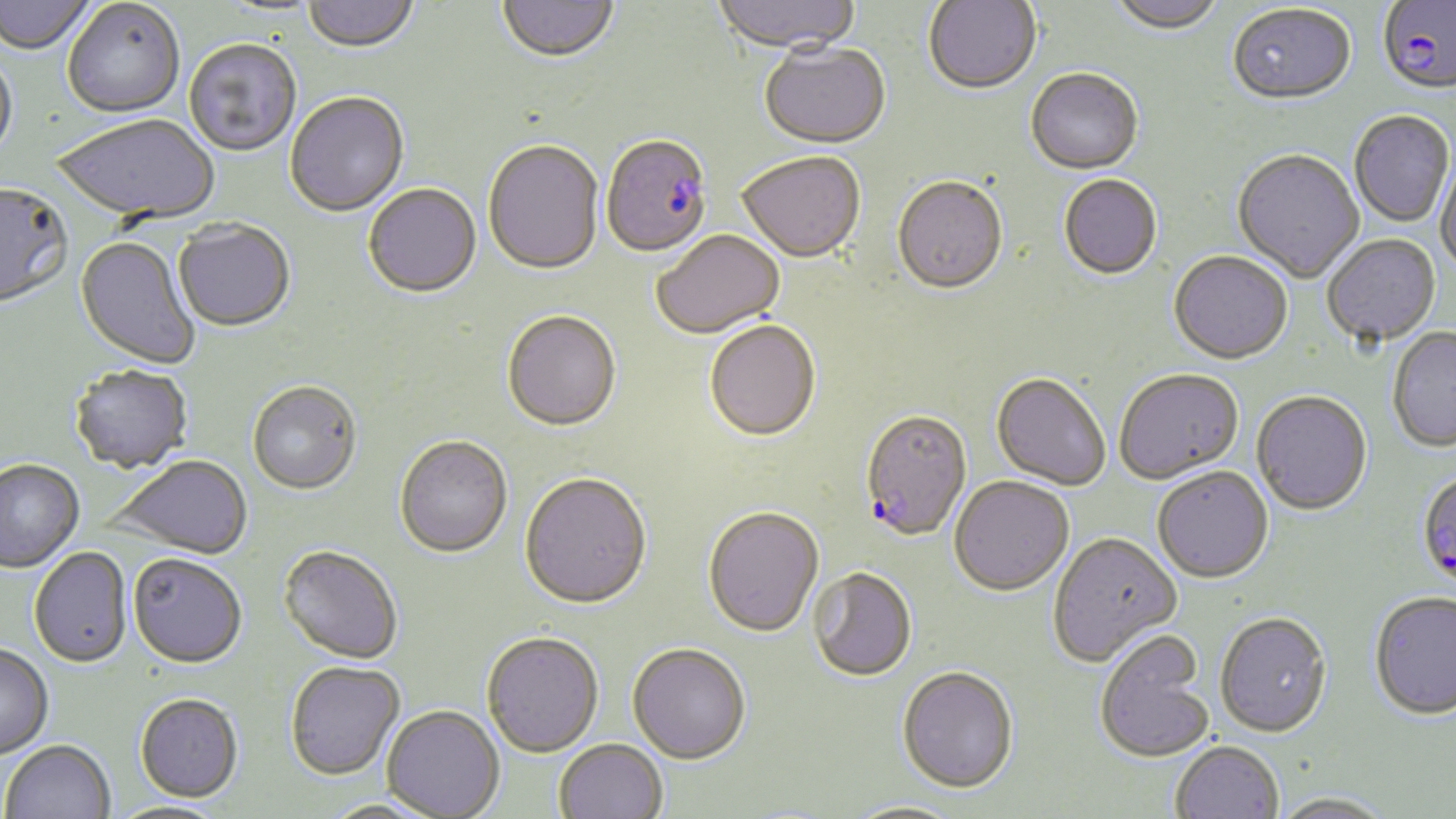

Approximate bounding boxes as named x1/y1/x2/y2 corners in pixels. Uninfected red blood cell locations: (x1=0, y1=0, x2=98, y2=57), (x1=304, y1=0, x2=418, y2=55), (x1=498, y1=0, x2=619, y2=66), (x1=711, y1=0, x2=863, y2=57), (x1=923, y1=0, x2=1042, y2=97), (x1=1108, y1=0, x2=1226, y2=37), (x1=62, y1=1, x2=185, y2=120), (x1=214, y1=1, x2=328, y2=20), (x1=1227, y1=6, x2=1356, y2=108), (x1=183, y1=41, x2=301, y2=158), (x1=759, y1=45, x2=891, y2=151), (x1=0, y1=55, x2=18, y2=170), (x1=1026, y1=71, x2=1144, y2=177), (x1=285, y1=94, x2=409, y2=219), (x1=1349, y1=113, x2=1454, y2=229), (x1=54, y1=117, x2=219, y2=225), (x1=483, y1=142, x2=604, y2=278), (x1=1232, y1=151, x2=1365, y2=284), (x1=1435, y1=152, x2=1456, y2=276), (x1=737, y1=154, x2=865, y2=265), (x1=1059, y1=176, x2=1162, y2=282), (x1=892, y1=179, x2=1008, y2=298), (x1=363, y1=185, x2=482, y2=301), (x1=0, y1=186, x2=73, y2=311), (x1=173, y1=221, x2=296, y2=334), (x1=652, y1=232, x2=786, y2=341), (x1=1322, y1=236, x2=1441, y2=348), (x1=74, y1=237, x2=200, y2=371), (x1=1168, y1=253, x2=1293, y2=367), (x1=502, y1=313, x2=621, y2=434), (x1=704, y1=322, x2=821, y2=444), (x1=1387, y1=328, x2=1456, y2=455), (x1=69, y1=366, x2=193, y2=475), (x1=1115, y1=371, x2=1243, y2=486), (x1=990, y1=374, x2=1110, y2=492), (x1=247, y1=383, x2=362, y2=496), (x1=1251, y1=393, x2=1373, y2=518), (x1=394, y1=438, x2=513, y2=560), (x1=107, y1=457, x2=253, y2=560), (x1=0, y1=461, x2=85, y2=574), (x1=1152, y1=468, x2=1274, y2=586), (x1=519, y1=475, x2=652, y2=612), (x1=949, y1=478, x2=1074, y2=598), (x1=703, y1=509, x2=824, y2=640), (x1=1048, y1=534, x2=1183, y2=669), (x1=278, y1=547, x2=403, y2=666), (x1=29, y1=548, x2=133, y2=670), (x1=127, y1=556, x2=247, y2=671), (x1=808, y1=569, x2=917, y2=684), (x1=1369, y1=595, x2=1456, y2=723), (x1=1215, y1=615, x2=1332, y2=741), (x1=1094, y1=633, x2=1213, y2=766), (x1=481, y1=634, x2=604, y2=759), (x1=0, y1=646, x2=54, y2=760), (x1=627, y1=646, x2=751, y2=767), (x1=285, y1=662, x2=405, y2=781), (x1=896, y1=669, x2=1019, y2=797), (x1=134, y1=695, x2=244, y2=804), (x1=382, y1=706, x2=504, y2=818), (x1=554, y1=740, x2=667, y2=819), (x1=2, y1=741, x2=116, y2=819), (x1=1171, y1=743, x2=1283, y2=819), (x1=1270, y1=795, x2=1397, y2=819), (x1=318, y1=799, x2=441, y2=819), (x1=842, y1=800, x2=966, y2=819). Plasmodium falciparum-infected red blood cell locations: (x1=1378, y1=2, x2=1455, y2=99), (x1=601, y1=136, x2=713, y2=260), (x1=859, y1=412, x2=972, y2=543), (x1=1416, y1=471, x2=1456, y2=595). Slide-level diagnosis: Plasmodium falciparum. May-Grünwald-Giemsa stain. One field of a larger specimen. Optical microscopy. Image is 1456×819 pixels. Captured at 1000x magnification. Thin blood smear.